Assess this cell for malaria.
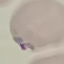
It is parasitized.

Summary:
  - Capture: smartphone camera at the microscope eyepiece
  - Preparation: thin smear
  - Image type: automatically extracted cell patch, resized to 64 × 64 pixels
  - Stain: Giemsa